Report the malaria status of this cell.
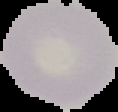
It is uninfected.

preparation: thin blood film
image_type: segmented cell region with the area outside set to black
image_size: 118×112 pixels